Point out each leukocyte.
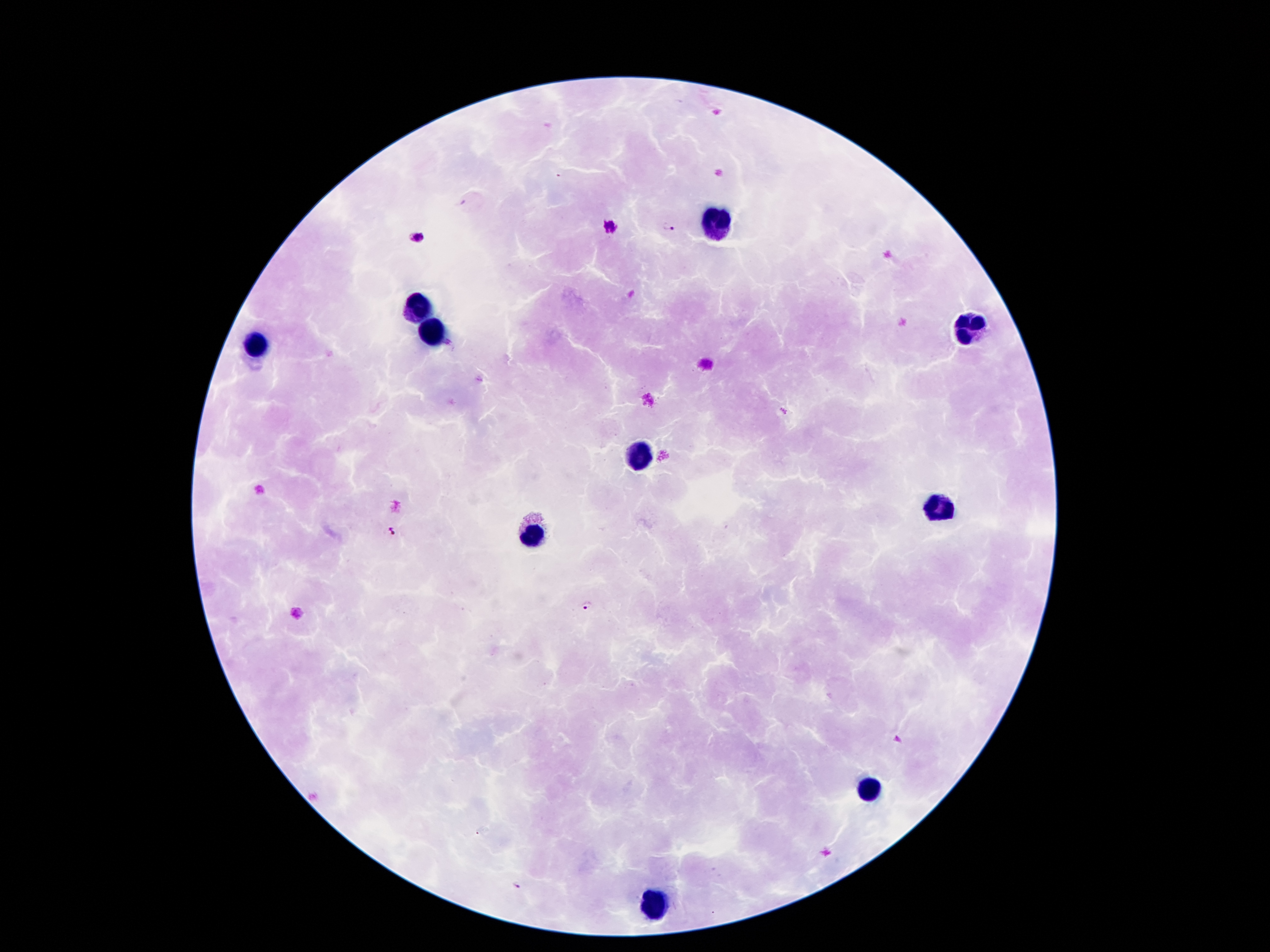
Approximate centers as (x, y) in pixels.
Leukocytes: (717, 225), (422, 307), (967, 324), (435, 333), (258, 344), (637, 458), (937, 503), (530, 536), (870, 788), (659, 902).

malaria parasite locations = (609, 225), (670, 227), (416, 236), (391, 532), (588, 605), (518, 886)
preparation = thick blood smear
stain = Giemsa
magnification = 100x
capture = smartphone camera through the microscope eyepiece
field of view = single
patient malaria status = infected with Plasmodium falciparum
image size = 1270×952 pixels